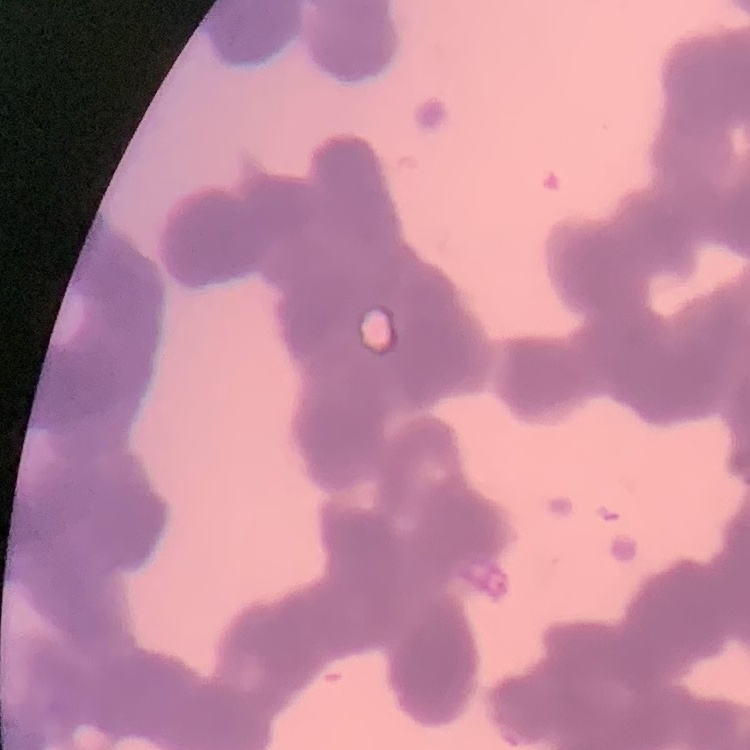

Summary:
  - Red blood cell morphology: rouleaux formation
  - Image type: one tile cut from a larger photomicrograph
  - Preparation: thin peripheral smear
  - Stain: Field's or Giemsa